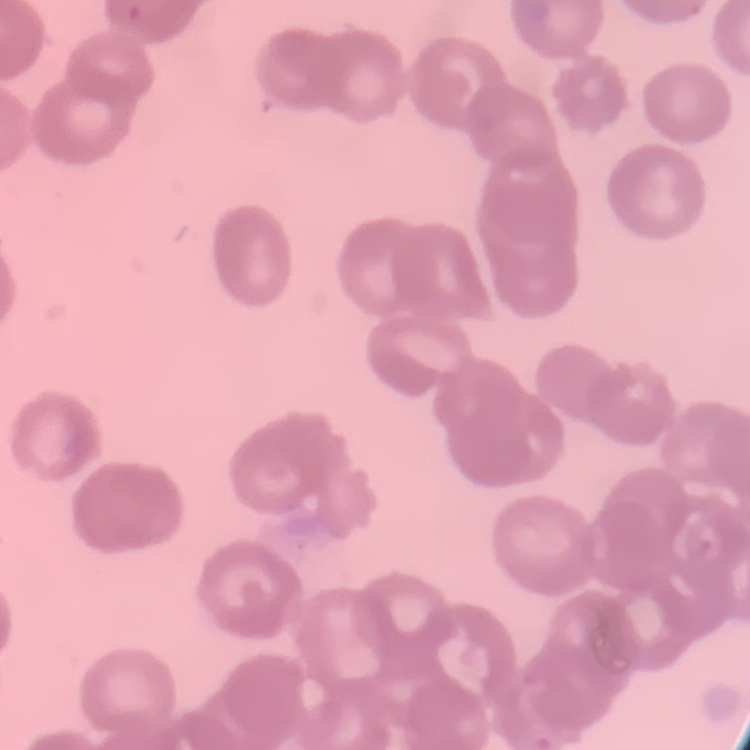
The red blood cells exhibit rouleaux formation. One tile cut from a larger photomicrograph. Field's or Giemsa stain. Thin blood smear.